Outline each Plasmodium falciparum-infected red blood cell.
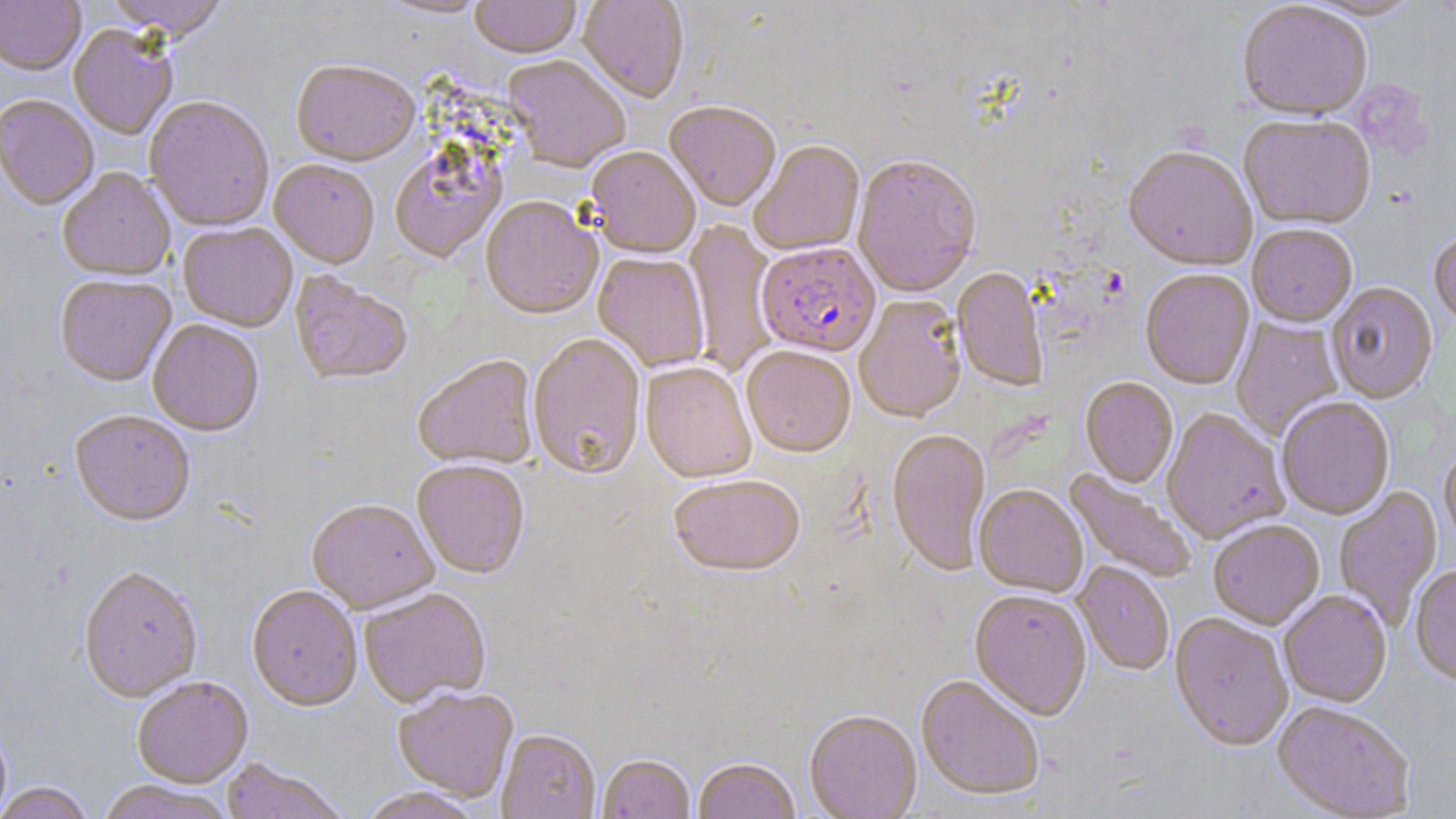
Approximate bounding boxes as [x1, y1, x2, y2] in pixels.
Plasmodium falciparum-infected red blood cells: [756, 243, 881, 359].

Uninfected red blood cell locations: [0, 0, 85, 78], [103, 0, 231, 44], [373, 0, 491, 20], [470, 0, 581, 61], [577, 0, 690, 105], [1298, 0, 1427, 23], [1237, 3, 1373, 124], [68, 26, 178, 141], [502, 57, 631, 174], [291, 63, 420, 169], [0, 97, 99, 212], [144, 98, 274, 233], [664, 104, 780, 214], [1238, 117, 1377, 232], [750, 142, 865, 258], [389, 148, 507, 265], [587, 148, 700, 261], [1123, 149, 1257, 274], [852, 158, 982, 299], [269, 162, 380, 270], [58, 169, 175, 283], [480, 198, 601, 322], [683, 219, 780, 375], [178, 224, 298, 333], [1247, 226, 1358, 329], [1429, 235, 1456, 332], [593, 254, 710, 372], [952, 269, 1048, 392], [1140, 271, 1255, 391], [289, 274, 413, 387], [55, 277, 176, 389], [1326, 284, 1438, 405], [855, 296, 967, 424], [1230, 315, 1343, 441], [148, 322, 264, 438], [528, 335, 646, 483], [741, 348, 856, 460], [413, 357, 539, 472], [641, 363, 756, 485], [1080, 379, 1178, 489], [1278, 398, 1395, 521], [1162, 410, 1289, 544], [69, 413, 195, 528], [887, 431, 991, 578], [1439, 448, 1456, 555], [412, 462, 529, 580], [1063, 470, 1197, 584], [668, 477, 806, 580], [974, 486, 1087, 598], [1333, 487, 1442, 631], [306, 501, 439, 616], [1209, 521, 1325, 631], [1072, 562, 1174, 677], [1410, 566, 1456, 688], [79, 568, 203, 705], [246, 587, 362, 713], [359, 589, 492, 709], [969, 592, 1091, 723], [1279, 592, 1392, 708], [1170, 615, 1293, 753], [915, 676, 1044, 802], [132, 678, 254, 789], [393, 687, 518, 802], [1272, 702, 1416, 818], [804, 712, 922, 819], [0, 723, 12, 819], [496, 731, 600, 819], [598, 756, 694, 819], [220, 759, 351, 819], [693, 760, 800, 819], [95, 781, 236, 819], [0, 783, 96, 819], [358, 788, 484, 819]. Slide-level diagnosis: Plasmodium falciparum. Image is 1456×819 pixels. Thin blood film. One field of a larger specimen. 1000x magnification. May-Grünwald-Giemsa stain. Optical microscopy.